Locate every blood parasite and identify its species.
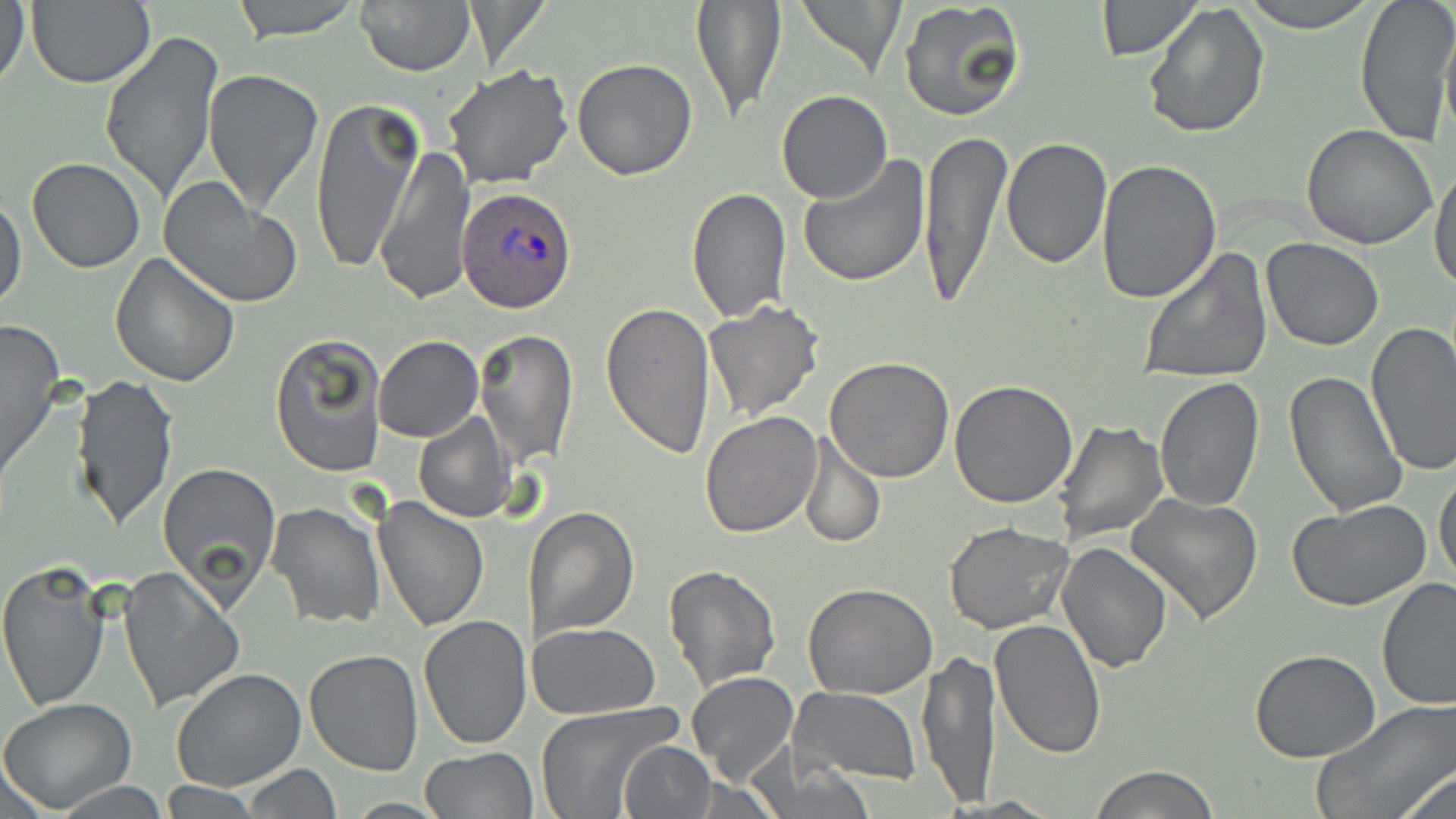
Approximate bounding boxes as (x1, y1, x2, y2) in pixels.
Plasmodium ovale-infected red blood cells: (458, 185, 579, 314).
No Plasmodium falciparum, Plasmodium malariae, Plasmodium vivax, Babesia divergens, or Trypanosoma brucei observed.

Summary:
  - Uninfected red blood cell locations: (1, 0, 31, 95), (230, 0, 363, 42), (355, 0, 474, 75), (794, 0, 907, 76), (1093, 0, 1202, 59), (1236, 0, 1383, 31), (1354, 0, 1456, 144), (25, 1, 156, 88), (689, 1, 787, 126), (899, 1, 1028, 123), (1142, 2, 1272, 141), (1439, 16, 1456, 152), (100, 29, 223, 203), (572, 57, 697, 180), (441, 63, 574, 191), (201, 69, 325, 214), (775, 91, 892, 205), (306, 95, 424, 278), (1302, 123, 1438, 248), (917, 129, 1013, 308), (1002, 135, 1113, 270), (376, 145, 476, 306), (796, 153, 931, 286), (26, 157, 146, 273), (1096, 160, 1222, 306), (1431, 161, 1456, 297), (160, 178, 303, 309), (687, 187, 791, 322), (0, 194, 27, 314), (1261, 237, 1383, 350), (1138, 247, 1273, 385), (110, 253, 240, 390), (602, 299, 716, 461), (701, 300, 825, 424), (0, 317, 64, 490), (1364, 323, 1456, 478), (473, 328, 579, 468), (269, 333, 386, 478), (373, 335, 483, 442), (824, 356, 955, 483), (1284, 370, 1407, 519), (70, 373, 179, 530), (1154, 375, 1265, 510), (948, 379, 1078, 507), (698, 411, 821, 539), (413, 413, 517, 524), (1052, 420, 1169, 543), (800, 433, 884, 550), (157, 461, 282, 602), (1433, 468, 1456, 593), (1125, 492, 1263, 624), (373, 497, 490, 632), (1287, 500, 1433, 612), (265, 501, 384, 630), (522, 504, 641, 641), (943, 522, 1075, 635), (1056, 541, 1174, 672), (0, 560, 111, 712), (663, 564, 782, 692), (117, 565, 244, 710), (1376, 576, 1456, 711), (802, 583, 937, 700), (418, 613, 532, 750), (990, 618, 1108, 758), (527, 622, 659, 719), (302, 647, 422, 775), (1249, 647, 1383, 762), (918, 649, 1001, 809), (171, 668, 306, 792), (686, 672, 798, 788), (790, 688, 921, 784), (0, 698, 137, 814), (1313, 700, 1455, 819), (535, 701, 684, 817), (617, 740, 717, 818), (419, 746, 540, 819), (1390, 763, 1456, 819), (243, 765, 340, 818), (1088, 765, 1220, 819), (51, 777, 169, 817), (160, 781, 259, 816)
  - Slide-level diagnosis: Plasmodium ovale
  - Stain: May-Grünwald-Giemsa
  - Image size: 1456×819 pixels
  - Preparation: thin blood film
  - Magnification: 1000x
  - Field of view: single
  - Modality: light microscopy